Classify this cell by malaria status.
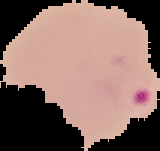
Parasitized.

image_size: 160×151 pixels
image_type: segmented cell region on a black background
preparation: thin blood smear